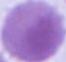
Summary:
  - Identification: erythrocyte
  - Magnification: 1000x
  - Modality: photomicrograph